Classify this cell by malaria status.
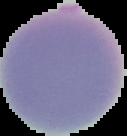
It is uninfected.

image size = 127×136 pixels
preparation = thin blood film
image type = segmented cell region on a black background